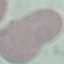

Summary:
  - Malaria status: uninfected
  - Stain: Giemsa
  - Image type: automatically extracted cell patch, resized to 64 × 64 pixels
  - Capture: smartphone through the microscope eyepiece
  - Preparation: thin smear